Report the malaria status of this cell.
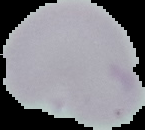

It is uninfected.

image type = segmented cell region on a black background
preparation = thin blood smear
image size = 145×130 pixels